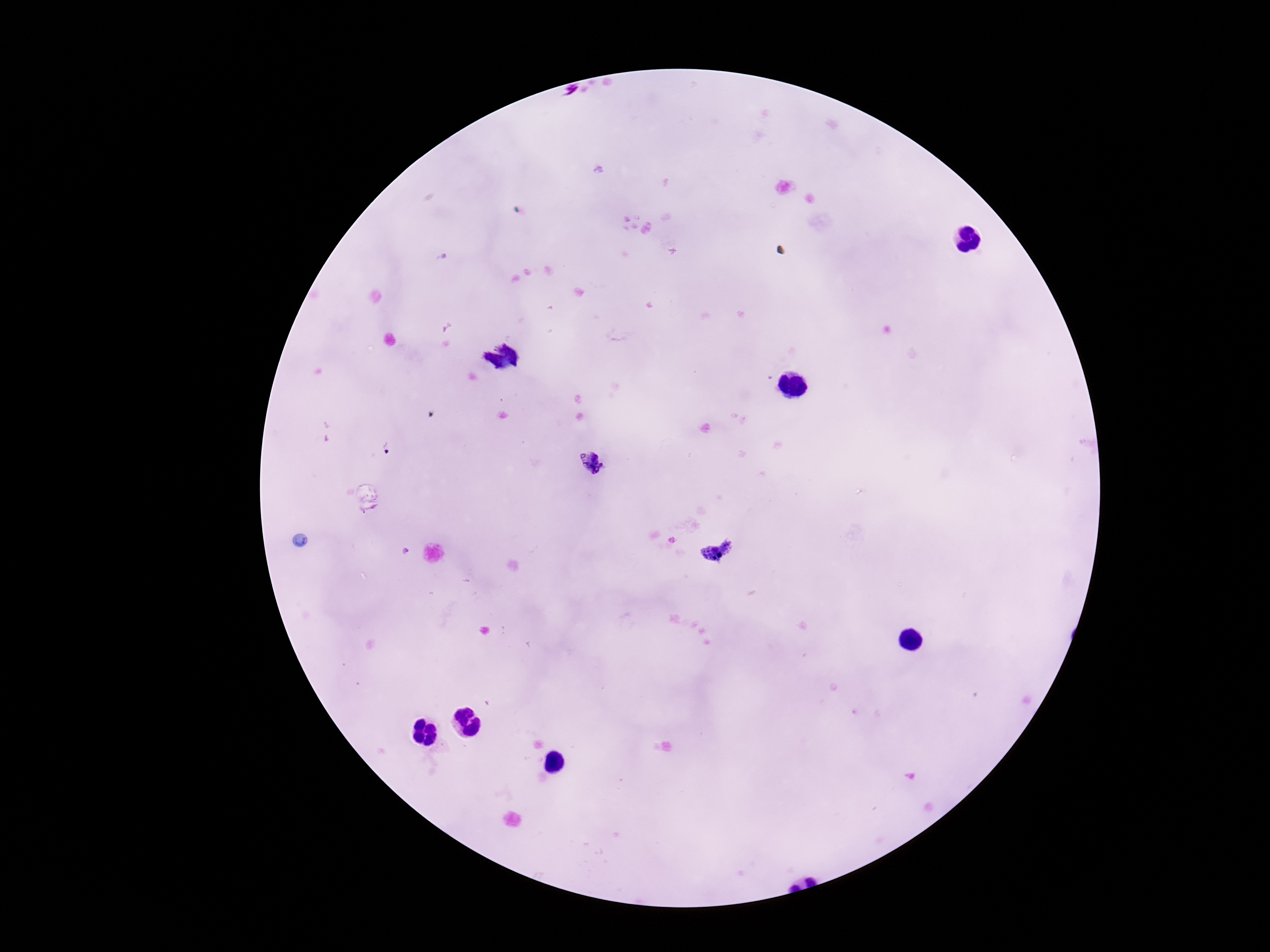

Approximate centers as {x, y} in pixels.
Summary:
  - Plasmodium parasite locations: {592, 462}, {718, 552}
  - Stain: Giemsa
  - Magnification: 100x
  - Patient malaria status: positive
  - Preparation: thick peripheral-blood smear
  - Capture: smartphone camera through the microscope eyepiece
  - Image size: 1270×952 pixels
  - Field of view: one from this slide